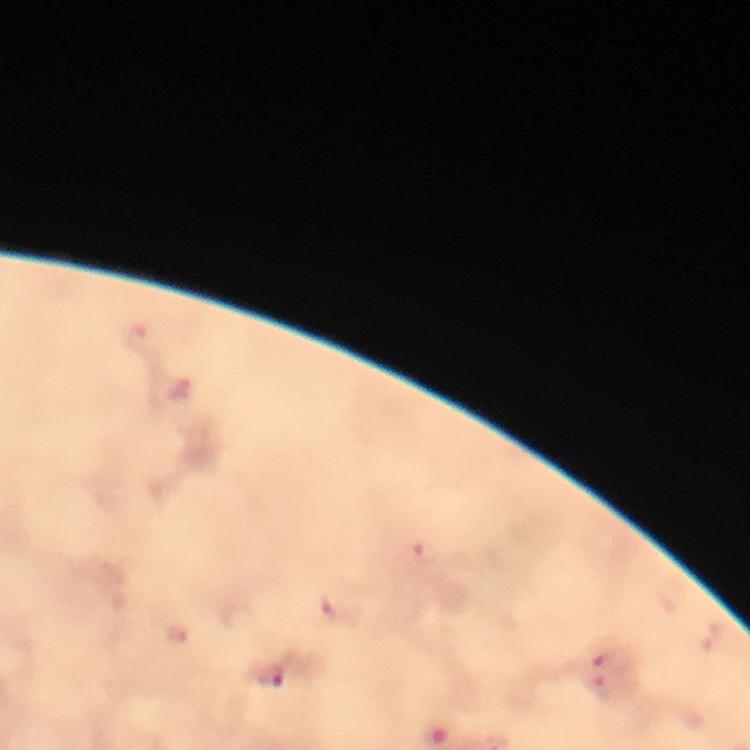

Approximate object centers, in pixels from the top-left corner.
Summary:
  - Plasmodium parasite locations: (x=425, y=554), (x=330, y=605), (x=179, y=633), (x=613, y=659), (x=270, y=677), (x=601, y=692)
  - Cropped from: a single field of view
  - Immersion oil: used
  - Context: from a malaria diagnostic workup
  - Stain: Giemsa
  - Preparation: thick blood film
  - Capture: smartphone photograph through a microscope
  - Magnification: 100x
  - Image size: 750×750 pixels